Report the malaria status of this cell.
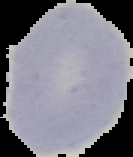
It is uninfected.

image type = segmented cell region on a black background
image size = 133×157 pixels
preparation = thin blood film